Describe the morphology of the red blood cells.
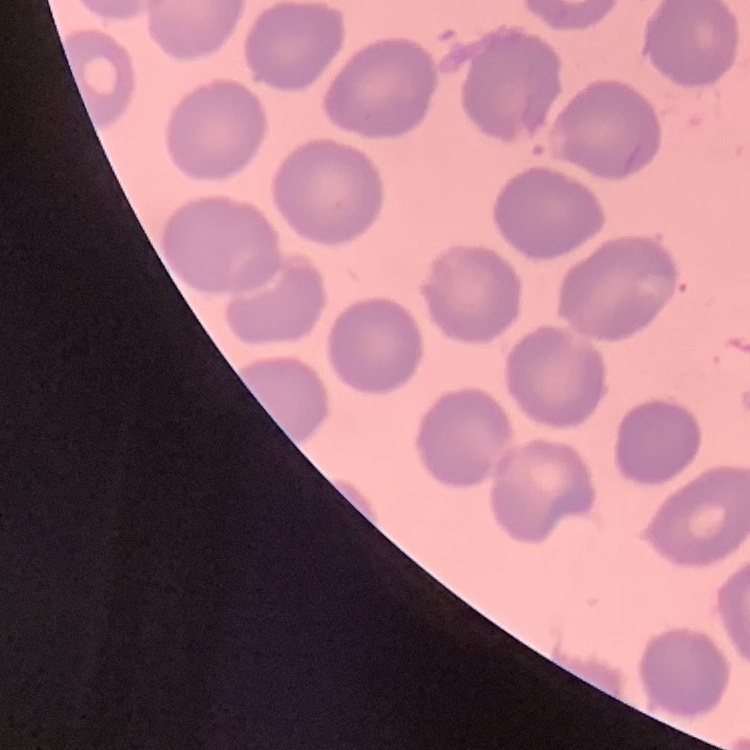
No rouleaux formation.

preparation = thin peripheral smear
image type = one tile cut from a larger photomicrograph
stain = Field's or Giemsa